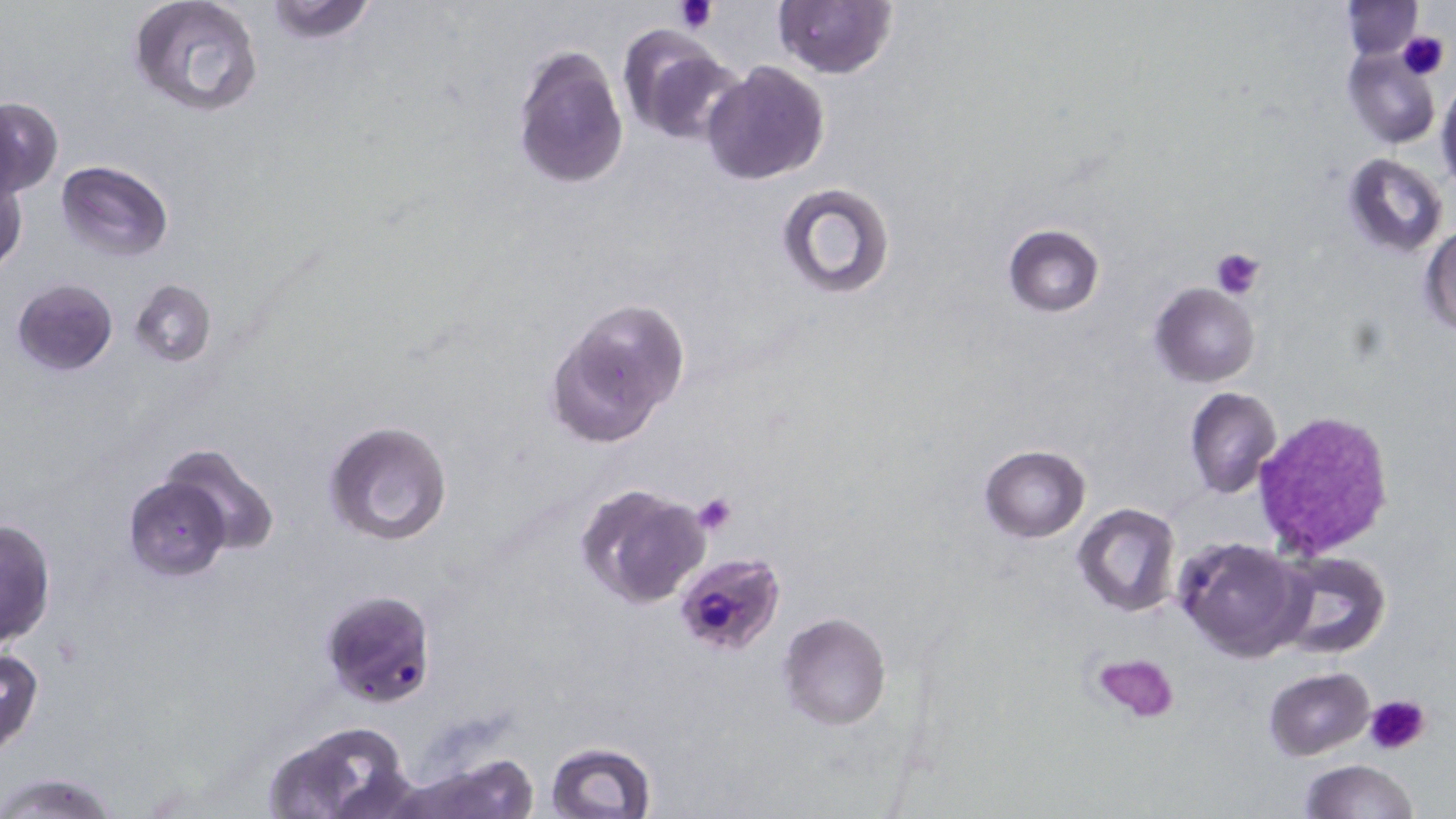

Summary:
  - Coordinate format: approximate bounding boxes as named x1/y1/x2/y2 corners in pixels
  - Plasmodium falciparum-infected red blood cell locations: (x1=667, y1=548, x2=787, y2=656), (x1=320, y1=588, x2=438, y2=707)
  - Uninfected red blood cell locations: (x1=127, y1=0, x2=264, y2=117), (x1=262, y1=0, x2=379, y2=45), (x1=774, y1=1, x2=896, y2=78), (x1=1344, y1=1, x2=1424, y2=58), (x1=616, y1=24, x2=740, y2=144), (x1=513, y1=42, x2=630, y2=191), (x1=1343, y1=47, x2=1439, y2=149), (x1=702, y1=61, x2=831, y2=186), (x1=1436, y1=78, x2=1456, y2=192), (x1=1, y1=97, x2=63, y2=196), (x1=1342, y1=152, x2=1449, y2=257), (x1=55, y1=160, x2=173, y2=262), (x1=1, y1=173, x2=28, y2=273), (x1=774, y1=181, x2=897, y2=301), (x1=1420, y1=224, x2=1455, y2=334), (x1=1002, y1=225, x2=1104, y2=316), (x1=11, y1=278, x2=118, y2=375), (x1=129, y1=279, x2=216, y2=367), (x1=1150, y1=282, x2=1261, y2=386), (x1=547, y1=299, x2=689, y2=449), (x1=1184, y1=387, x2=1282, y2=498), (x1=323, y1=419, x2=454, y2=546), (x1=154, y1=442, x2=280, y2=557), (x1=978, y1=445, x2=1089, y2=542), (x1=123, y1=476, x2=232, y2=579), (x1=577, y1=484, x2=712, y2=608), (x1=1074, y1=504, x2=1180, y2=617), (x1=0, y1=519, x2=56, y2=649), (x1=1174, y1=535, x2=1311, y2=663), (x1=1275, y1=550, x2=1390, y2=660), (x1=779, y1=612, x2=891, y2=729), (x1=0, y1=648, x2=45, y2=758), (x1=1264, y1=666, x2=1375, y2=760), (x1=260, y1=727, x2=412, y2=818), (x1=544, y1=741, x2=658, y2=819), (x1=408, y1=752, x2=543, y2=819), (x1=1300, y1=759, x2=1419, y2=818), (x1=0, y1=770, x2=121, y2=818)
  - Platelet locations: (x1=675, y1=0, x2=717, y2=34), (x1=1397, y1=32, x2=1450, y2=80), (x1=1210, y1=247, x2=1267, y2=299), (x1=1252, y1=410, x2=1394, y2=557), (x1=692, y1=491, x2=738, y2=535), (x1=1091, y1=652, x2=1179, y2=724), (x1=1365, y1=694, x2=1430, y2=757)
  - Slide-level diagnosis: Plasmodium falciparum
  - Stain: May-Grünwald-Giemsa
  - Preparation: thin blood smear
  - Modality: optical microscopy
  - Image size: 1456×819 pixels
  - Field of view: one of a larger specimen
  - Magnification: 1000x